State which parasite is depicted.
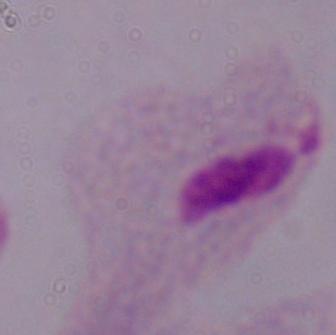

This is a trichomonad.

1000x magnification. Photomicrograph.